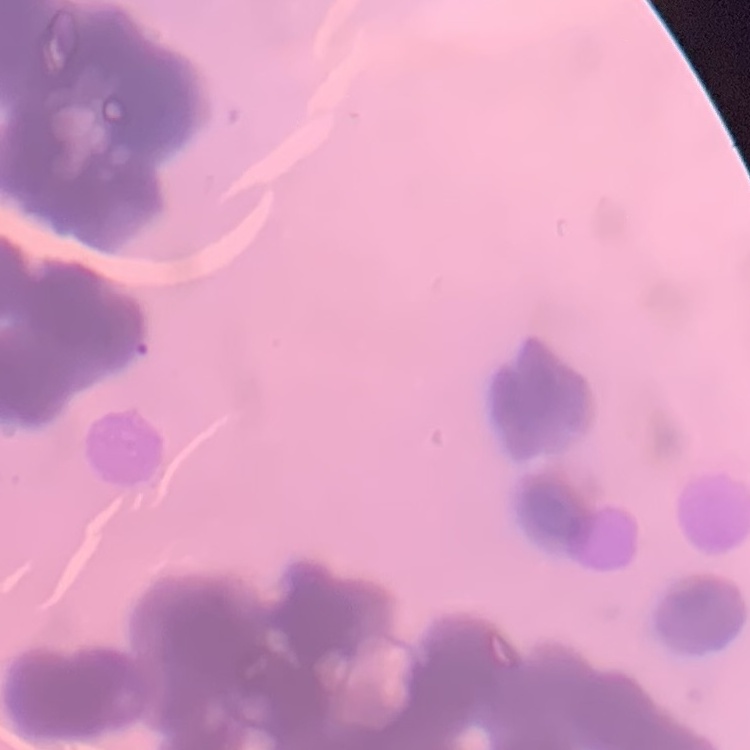
red blood cell morphology = rouleaux formation
preparation = thin blood film
stain = Field's or Giemsa
image type = one tile cut from a larger photomicrograph